Outline each blood parasite and name the species.
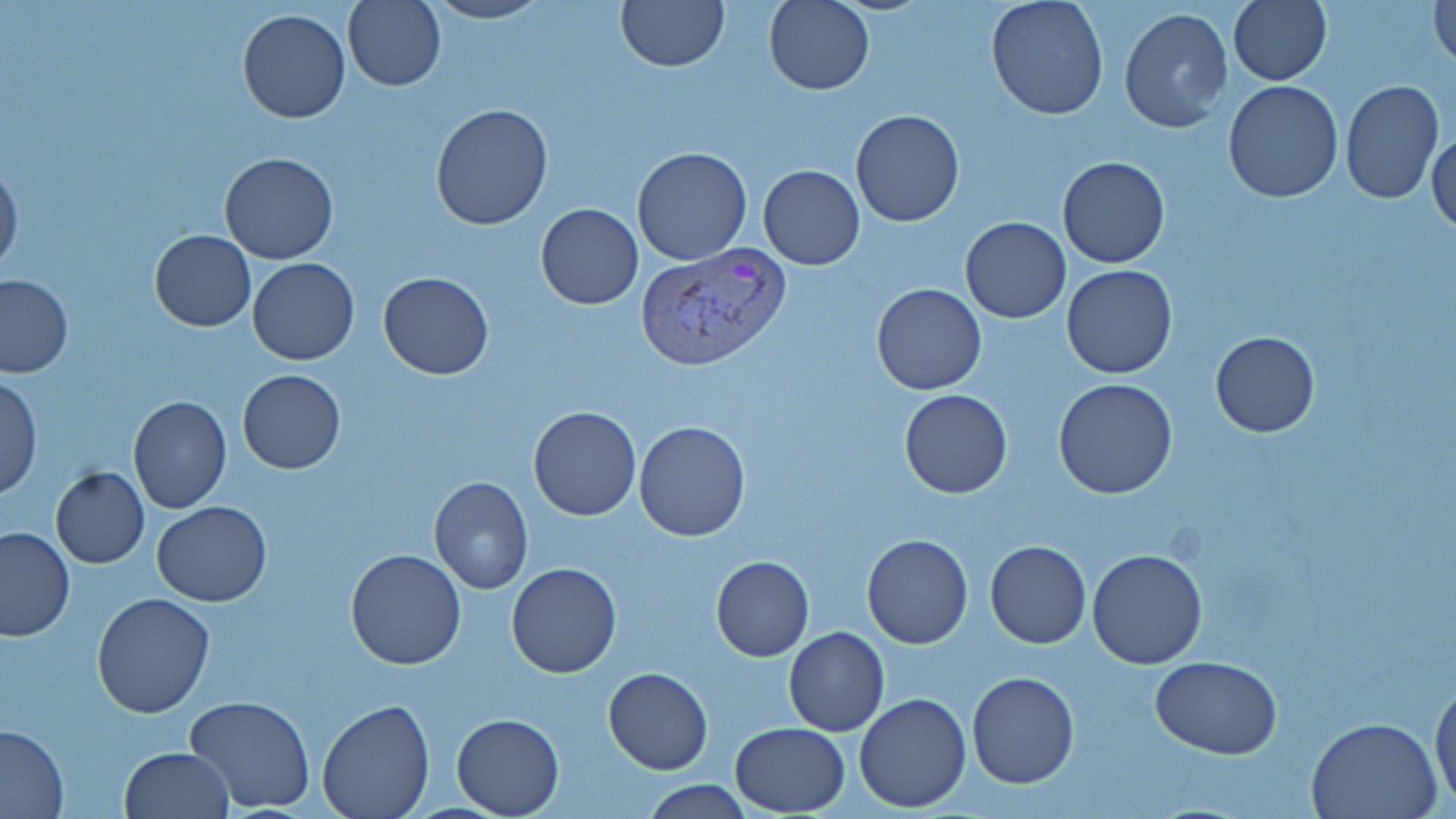

Approximate bounding boxes as (x1,y1)-(x2,y2) corner pairs in pixels.
Plasmodium vivax-infected red blood cells: (635,244)-(793,373).
No Plasmodium falciparum, Plasmodium ovale, Plasmodium malariae, Babesia divergens, or Trypanosoma brucei observed.

slide-level diagnosis = Plasmodium vivax
stain = May-Grünwald-Giemsa
image size = 1456×819 pixels
uninfected red blood cell locations = approximate bounding boxes as (x1,y1)-(x2,y2) corner pairs in pixels: (423,0)-(552,25), (615,0)-(728,71), (764,0)-(875,93), (986,0)-(1109,120), (1228,0)-(1332,86), (1430,0)-(1455,68), (343,1)-(447,92), (1118,6)-(1233,132), (237,9)-(350,123), (1223,81)-(1344,203), (1339,82)-(1444,203), (430,102)-(555,231), (849,110)-(964,228), (1427,128)-(1456,236), (630,146)-(753,266), (219,152)-(338,265), (1057,156)-(1170,269), (0,160)-(23,276), (758,164)-(865,269), (536,203)-(644,310), (960,216)-(1071,322), (149,230)-(256,331), (248,256)-(360,365), (1062,265)-(1179,379), (378,272)-(494,379), (0,274)-(73,378), (872,283)-(986,394), (1209,330)-(1319,438), (238,370)-(345,474), (1,374)-(41,500), (1053,378)-(1179,499), (899,389)-(1013,499), (127,395)-(232,513), (528,405)-(641,521), (632,420)-(751,543), (50,466)-(149,568), (429,476)-(532,594), (152,501)-(272,605), (0,525)-(74,642), (861,534)-(973,650), (985,540)-(1091,648), (1087,548)-(1208,669), (346,549)-(467,669), (710,555)-(814,661), (506,564)-(623,679), (92,594)-(214,717), (784,627)-(889,736), (1152,655)-(1281,758), (603,667)-(712,775), (1429,669)-(1455,812), (967,673)-(1080,789), (854,692)-(972,813), (183,694)-(317,814), (316,699)-(434,818), (451,714)-(563,817), (1306,716)-(1445,819), (729,721)-(850,815), (0,726)-(69,818), (119,747)-(234,819), (638,780)-(760,817)
modality = optical microscopy
field of view = one of a larger specimen
magnification = 1000x
preparation = thin blood film